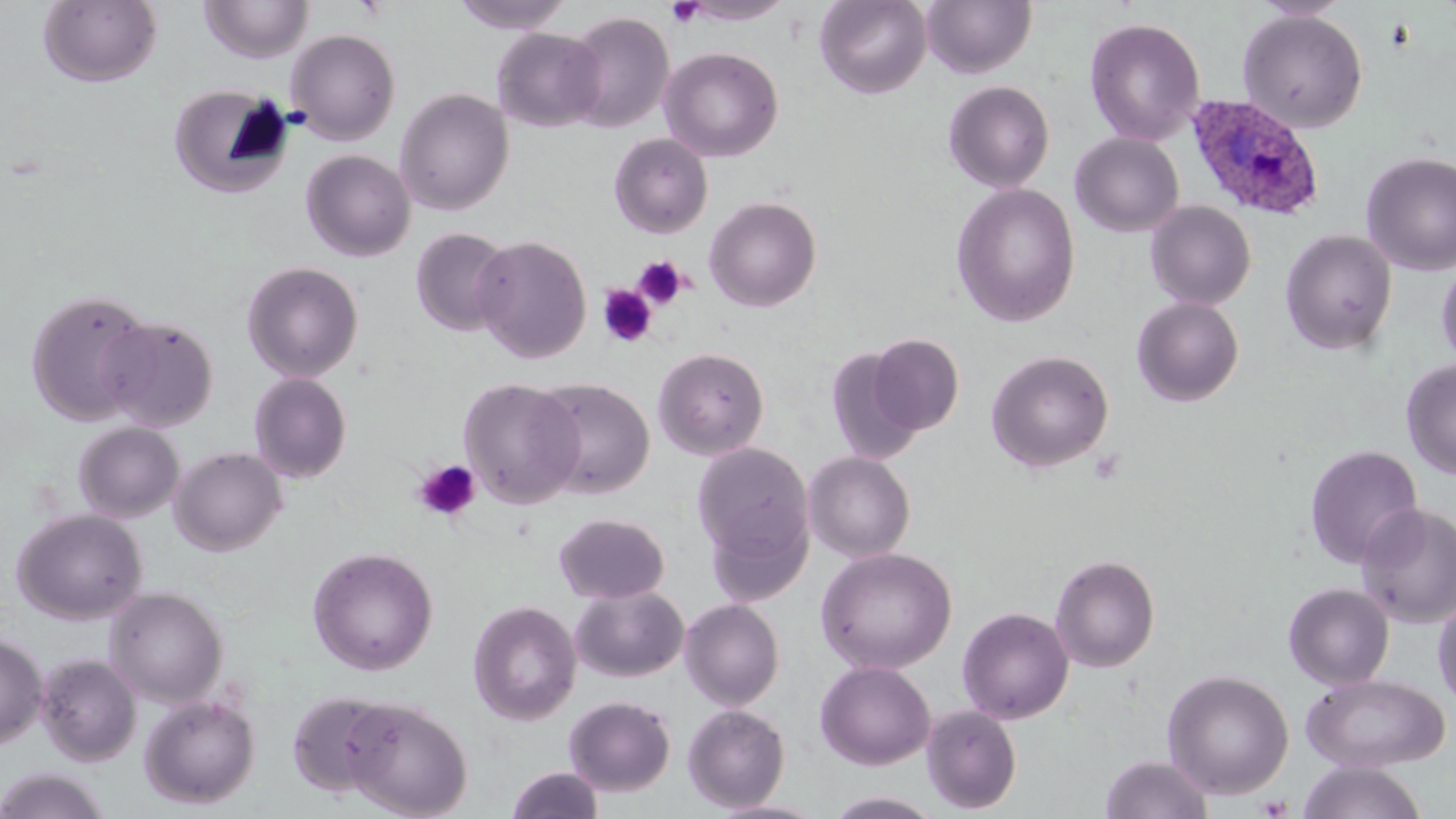

{
  "slide_level_diagnosis": "Plasmodium ovale",
  "uninfected_red_blood_cell_locations": "approximate bounding boxes as named x1/y1/x2/y2 corners in pixels: (x1=38, y1=0, x2=162, y2=88), (x1=450, y1=0, x2=574, y2=33), (x1=681, y1=0, x2=793, y2=25), (x1=815, y1=0, x2=932, y2=98), (x1=922, y1=0, x2=1036, y2=78), (x1=199, y1=1, x2=313, y2=64), (x1=1253, y1=1, x2=1352, y2=21), (x1=1238, y1=9, x2=1368, y2=133), (x1=564, y1=11, x2=674, y2=133), (x1=1084, y1=17, x2=1205, y2=146), (x1=492, y1=27, x2=607, y2=132), (x1=286, y1=28, x2=401, y2=145), (x1=660, y1=46, x2=784, y2=162), (x1=943, y1=80, x2=1055, y2=193), (x1=167, y1=83, x2=295, y2=199), (x1=394, y1=87, x2=514, y2=215), (x1=1070, y1=132, x2=1184, y2=237), (x1=609, y1=133, x2=713, y2=238), (x1=300, y1=149, x2=416, y2=262), (x1=1361, y1=152, x2=1456, y2=275), (x1=951, y1=183, x2=1081, y2=327), (x1=704, y1=195, x2=822, y2=312), (x1=1145, y1=201, x2=1256, y2=310), (x1=411, y1=227, x2=514, y2=337), (x1=1280, y1=229, x2=1397, y2=355), (x1=473, y1=235, x2=592, y2=363), (x1=1436, y1=260, x2=1456, y2=369), (x1=241, y1=261, x2=363, y2=382), (x1=25, y1=289, x2=154, y2=427), (x1=1132, y1=297, x2=1245, y2=407), (x1=99, y1=315, x2=220, y2=432), (x1=868, y1=334, x2=965, y2=435), (x1=653, y1=346, x2=770, y2=460), (x1=824, y1=347, x2=925, y2=465), (x1=986, y1=350, x2=1114, y2=472), (x1=1401, y1=358, x2=1456, y2=480), (x1=249, y1=372, x2=352, y2=483), (x1=459, y1=377, x2=583, y2=508), (x1=531, y1=378, x2=655, y2=499), (x1=73, y1=421, x2=184, y2=522), (x1=692, y1=441, x2=814, y2=568), (x1=1304, y1=444, x2=1423, y2=569), (x1=170, y1=446, x2=286, y2=556), (x1=803, y1=451, x2=916, y2=562), (x1=1356, y1=503, x2=1456, y2=628), (x1=704, y1=505, x2=813, y2=608), (x1=12, y1=508, x2=148, y2=625), (x1=555, y1=513, x2=670, y2=603), (x1=307, y1=546, x2=438, y2=675), (x1=816, y1=547, x2=957, y2=674), (x1=1050, y1=554, x2=1160, y2=673), (x1=1284, y1=582, x2=1395, y2=690), (x1=571, y1=585, x2=689, y2=682), (x1=106, y1=586, x2=228, y2=707), (x1=1432, y1=592, x2=1456, y2=714), (x1=680, y1=599, x2=785, y2=711), (x1=468, y1=600, x2=582, y2=725), (x1=957, y1=607, x2=1074, y2=724), (x1=0, y1=631, x2=48, y2=749), (x1=37, y1=653, x2=141, y2=766), (x1=815, y1=660, x2=936, y2=770), (x1=1162, y1=669, x2=1294, y2=799), (x1=1301, y1=673, x2=1451, y2=772), (x1=286, y1=690, x2=395, y2=797), (x1=139, y1=693, x2=260, y2=809), (x1=564, y1=695, x2=676, y2=795), (x1=342, y1=697, x2=473, y2=818), (x1=682, y1=704, x2=790, y2=812), (x1=921, y1=705, x2=1022, y2=814), (x1=1101, y1=753, x2=1213, y2=819), (x1=1297, y1=760, x2=1428, y2=819), (x1=506, y1=766, x2=604, y2=819), (x1=0, y1=769, x2=112, y2=818), (x1=824, y1=791, x2=947, y2=818), (x1=708, y1=799, x2=831, y2=819)",
  "plasmodium_ovale_infected_red_blood_cell_locations": "approximate bounding boxes as named x1/y1/x2/y2 corners in pixels: (x1=1187, y1=94, x2=1324, y2=219)",
  "image_size": "1456×819 pixels",
  "platelet_locations": "approximate bounding boxes as named x1/y1/x2/y2 corners in pixels: (x1=666, y1=0, x2=704, y2=27), (x1=632, y1=255, x2=689, y2=311), (x1=598, y1=284, x2=657, y2=347), (x1=1088, y1=449, x2=1126, y2=485), (x1=413, y1=460, x2=481, y2=521), (x1=1258, y1=795, x2=1291, y2=818)",
  "preparation": "thin blood smear",
  "field_of_view": "single",
  "magnification": "1000x",
  "stain": "May-Grünwald-Giemsa",
  "modality": "optical microscopy"
}